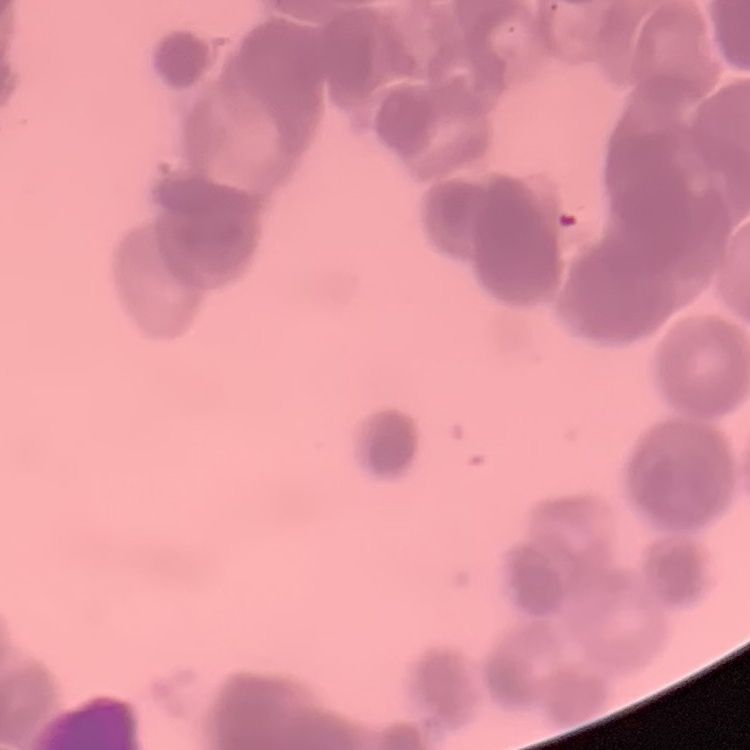 The red blood cells show rouleaux formation. Field's or Giemsa stain. Thin peripheral smear. Square crop of a larger photomicrograph.